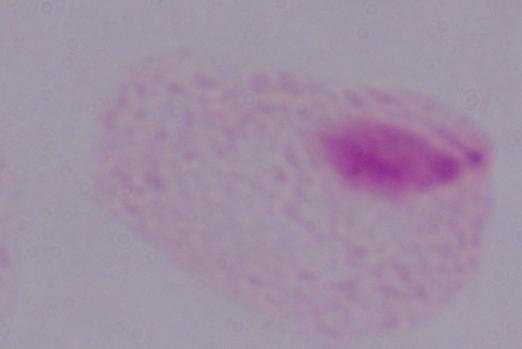
{
  "magnification": "1000x",
  "modality": "micrograph",
  "identification": "trichomonad"
}